Describe the morphology of the erythrocytes.
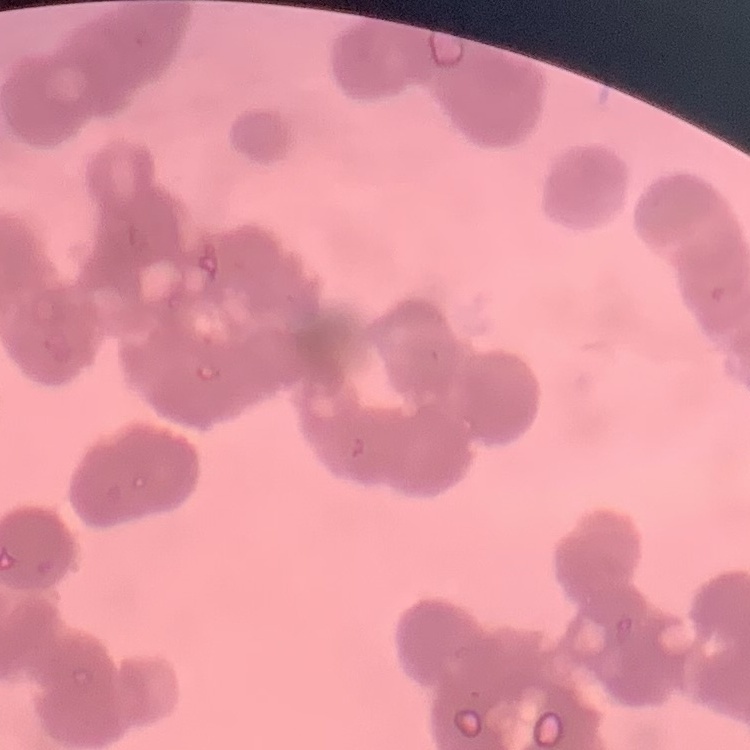
They show rouleaux formation.

Summary:
  - Preparation: thin blood smear
  - Stain: Field's or Giemsa
  - Image type: square crop of a larger photomicrograph